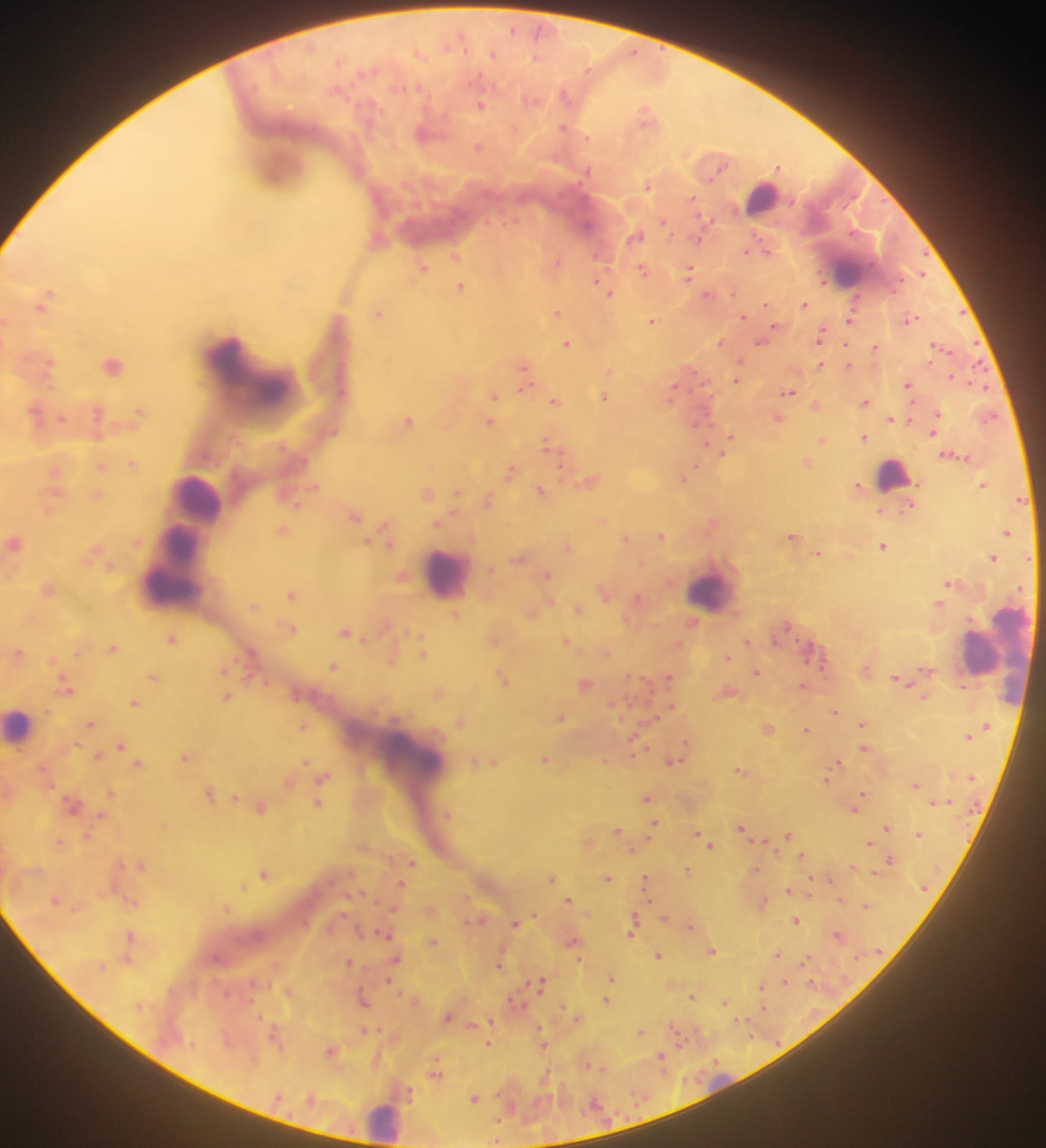

malaria parasite locations = approximate centers as x y in pixels: 513 29; 419 53; 492 55; 536 57; 566 95; 531 99; 481 105; 646 115; 564 127; 515 129; 426 132; 477 147; 777 167; 647 185; 691 199; 663 221; 635 235; 698 238; 377 240; 746 251; 765 251; 456 255; 557 260; 421 267; 642 269; 688 272; 921 273; 822 280; 598 281; 460 286; 602 287; 732 292; 608 293; 707 294; 45 299; 854 300; 766 304; 803 304; 556 312; 379 313; 743 317; 909 318; 850 319; 652 320; 6 321; 776 326; 820 335; 720 342; 760 342; 567 344; 845 344; 935 344; 875 346; 740 361; 47 362; 112 364; 819 364; 847 366; 524 367; 609 370; 951 377; 736 379; 524 380; 908 384; 673 390; 788 391; 494 395; 604 397; 554 401; 865 401; 815 404; 139 410; 35 413; 97 414; 936 414; 989 415; 60 417; 777 417; 891 419; 407 420; 489 422; 697 424; 934 425; 932 432; 729 437; 864 437; 821 439; 548 443; 722 453; 952 456; 132 462; 806 462; 102 465; 695 465; 510 470; 55 471; 683 477; 589 481; 983 484; 314 486; 858 486; 540 490; 426 492; 456 493; 97 494; 487 500; 1020 500; 908 507; 49 510; 879 511; 354 513; 602 520; 712 523; 436 524; 283 530; 1006 533; 661 534; 792 536; 387 537; 625 538; 13 542; 367 542; 882 546; 568 547; 93 551; 818 553; 519 557; 992 558; 109 565; 490 568; 402 574; 546 575; 949 582; 46 588; 604 591; 291 594; 637 598; 938 603; 253 605; 578 609; 531 612; 456 615; 626 620; 384 625; 291 628; 345 631; 172 638; 493 640; 565 641; 747 642; 677 644; 112 648; 77 652; 606 652; 16 653; 423 653; 726 656; 53 659; 392 659; 333 665; 224 668; 755 671; 153 676; 629 676; 502 678; 668 678; 896 679; 265 682; 584 683; 66 685; 803 686; 438 692; 726 692; 226 697; 924 697; 135 703; 613 703; 671 706; 47 710; 834 712; 655 717; 560 718; 460 720; 91 723; 862 724; 303 725; 767 728; 805 730; 967 736; 687 743; 635 744; 121 745; 681 748; 864 748; 186 755; 97 756; 545 758; 672 760; 604 761; 305 762; 475 762; 490 762; 838 763; 137 764; 832 769; 739 770; 323 776; 826 778; 288 781; 915 784; 111 791; 862 793; 209 794; 234 797; 647 798; 318 802; 72 803; 936 803; 260 806; 854 807; 447 813; 100 815; 653 822; 741 826; 887 826; 617 829; 788 834; 918 834; 86 835; 698 835; 648 838; 764 841; 59 842; 586 842; 870 842; 708 843; 362 847; 632 850; 801 855; 890 858; 412 862; 140 864; 853 866; 686 869; 755 870; 263 872; 875 872; 552 877; 606 877; 828 878; 645 880; 401 884; 243 886; 787 890; 809 894; 55 899; 568 899; 841 900; 763 901; 866 907; 226 908; 393 908; 429 909; 533 914; 664 918; 476 920; 634 920; 796 920; 514 923; 689 926; 359 930; 632 932; 130 935; 385 935; 838 935; 572 940; 433 942; 711 951; 657 954; 777 954; 396 959; 805 959; 126 960; 500 961; 348 962; 612 977; 389 980; 783 982; 540 983; 761 985; 287 990; 226 992; 692 996; 363 999; 414 1000; 605 1000; 515 1001; 724 1002; 762 1007; 258 1016; 448 1016; 577 1019; 490 1020; 741 1021; 471 1025; 364 1029; 675 1030; 640 1031; 277 1038; 678 1041; 489 1044; 543 1045; 331 1050; 375 1058; 660 1060; 601 1068; 435 1072; 545 1077; 475 1097; 312 1098; 497 1119; 498 1127; 497 1140
preparation = thick blood smear
field of view = single
image size = 1046×1148 pixels
country = Ghana
capture = mobile-phone photograph through a microscope
leukocyte locations = approximate centers as x y in pixels: 278 167; 762 198; 847 270; 234 365; 892 475; 195 499; 169 571; 445 572; 710 592; 999 654; 984 655; 19 726; 412 760; 383 1121